Classify this cell by malaria status.
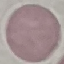
It is uninfected.

Cell patch, automatically extracted from a larger field of view and resized to 64 × 64 pixels. Thin blood film. Acquired by smartphone through the microscope eyepiece. Giemsa-stained preparation.